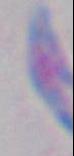
Captured at 1000x magnification. Toxoplasma gondii is seen. Micrograph.